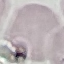 Result: negative for malaria parasites. Automatically extracted cell patch, resized to 64 × 64 pixels. Thin smear of blood. Giemsa-stained preparation. Acquired by smartphone through the microscope eyepiece.